Locate and identify every blood parasite.
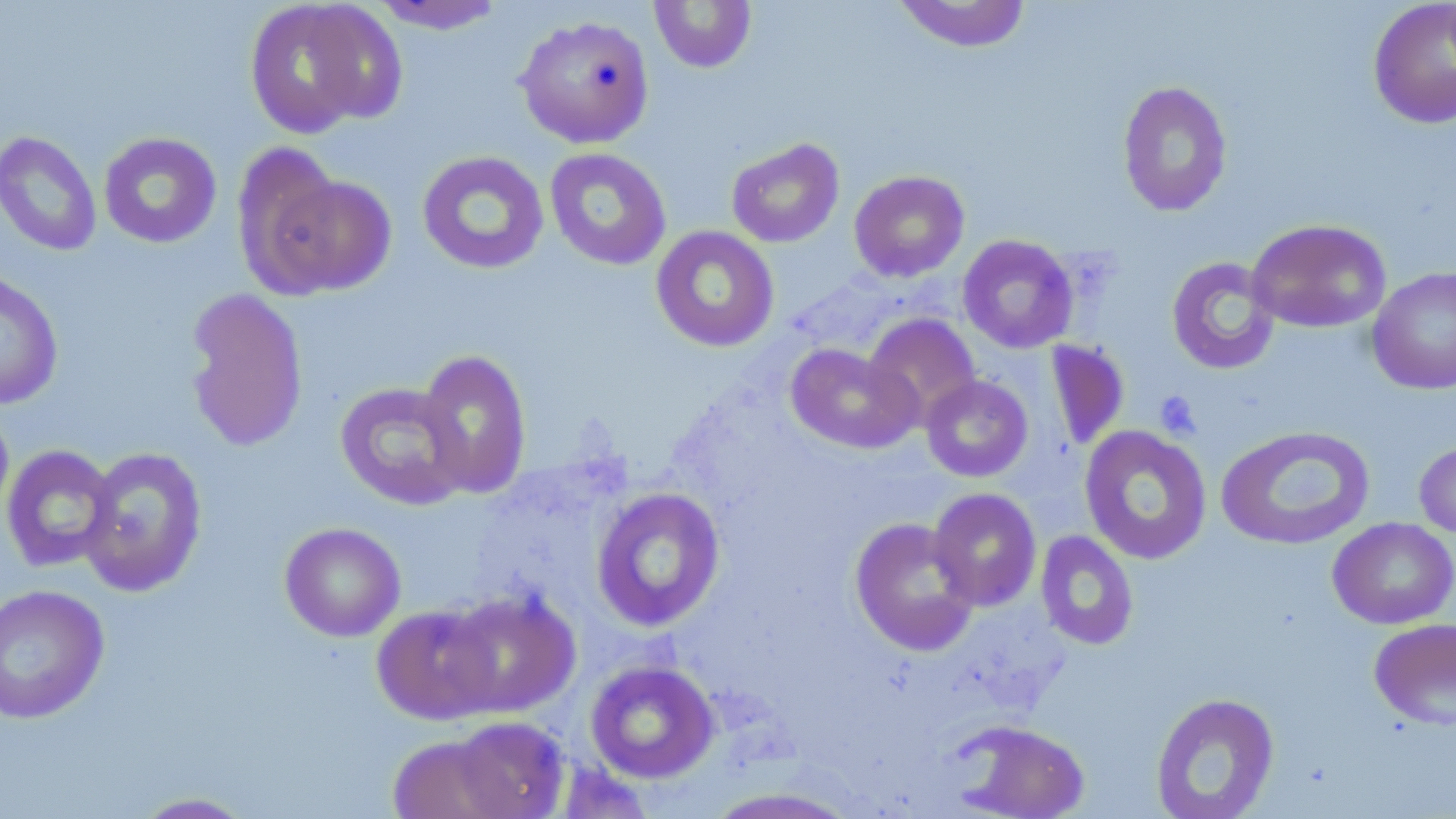
No blood parasites seen.

Approximate bounding boxes as [x1, y1, x2, y2] in pixels. Platelet locations: [1154, 390, 1202, 440]. Uninfected red blood cell locations: [892, 0, 1033, 53], [1367, 0, 1456, 129], [244, 1, 404, 137], [367, 1, 508, 35], [649, 1, 757, 73], [514, 14, 655, 149], [1117, 81, 1233, 217], [0, 131, 102, 257], [98, 132, 222, 248], [726, 138, 845, 248], [544, 148, 672, 270], [417, 150, 549, 275], [243, 161, 397, 301], [849, 170, 969, 282], [1247, 219, 1391, 334], [650, 225, 779, 353], [957, 235, 1079, 354], [1166, 256, 1281, 376], [1366, 266, 1456, 395], [0, 269, 64, 410], [184, 288, 309, 453], [863, 313, 981, 428], [1045, 339, 1130, 451], [785, 343, 920, 454], [415, 348, 532, 499], [921, 375, 1033, 482], [334, 381, 471, 509], [0, 401, 14, 528], [1216, 425, 1376, 551], [1079, 426, 1213, 565], [1414, 437, 1456, 540], [1, 445, 119, 573], [78, 446, 208, 598], [591, 487, 726, 631], [927, 487, 1042, 611], [849, 517, 980, 655], [1327, 517, 1456, 629], [279, 522, 406, 642], [1035, 530, 1139, 650], [0, 583, 110, 724], [441, 588, 580, 719], [371, 604, 502, 725], [1369, 618, 1456, 730], [585, 660, 720, 783], [1150, 692, 1279, 818], [446, 715, 570, 818], [951, 720, 1090, 819], [387, 733, 514, 819], [704, 787, 861, 819], [128, 792, 259, 818]. Slide-level diagnosis: negative for blood parasites. Optical microscopy. Captured at 1000x magnification. Thin blood film. One field of a larger specimen. Image is 1456×819 pixels. May-Grünwald-Giemsa-stained preparation.